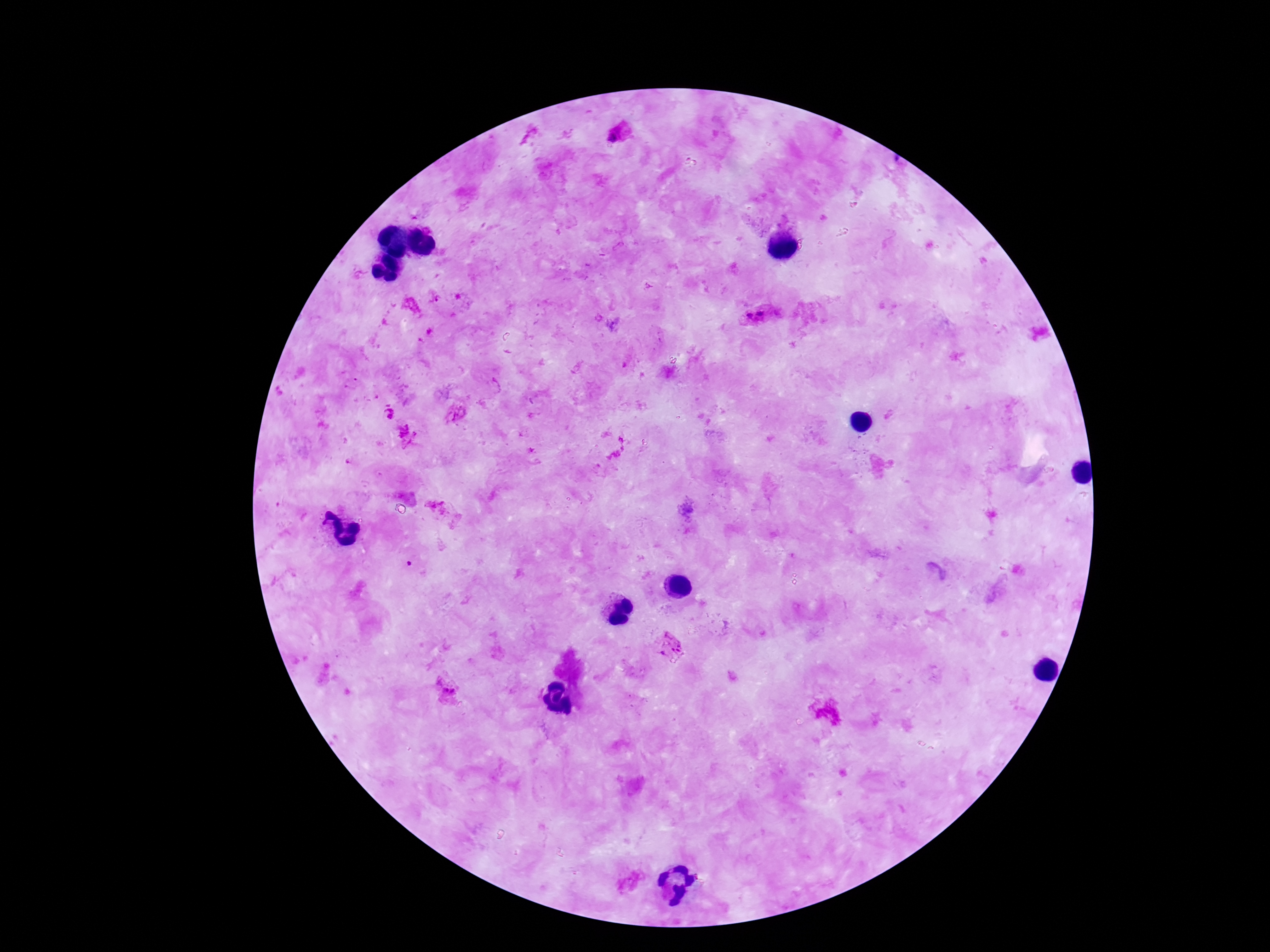
Approximate centers as [x, y] in pixels.
Summary:
  - Plasmodium parasite locations: [615, 136], [436, 297], [412, 306], [761, 313], [750, 316], [389, 404], [388, 414], [457, 415], [407, 435], [437, 507], [672, 646], [447, 688]
  - Image size: 1270×952 pixels
  - Field of view: single
  - Preparation: thick peripheral-blood smear
  - Capture: smartphone camera through the microscope eyepiece
  - Stain: Giemsa
  - Magnification: 100x
  - Patient malaria status: infected